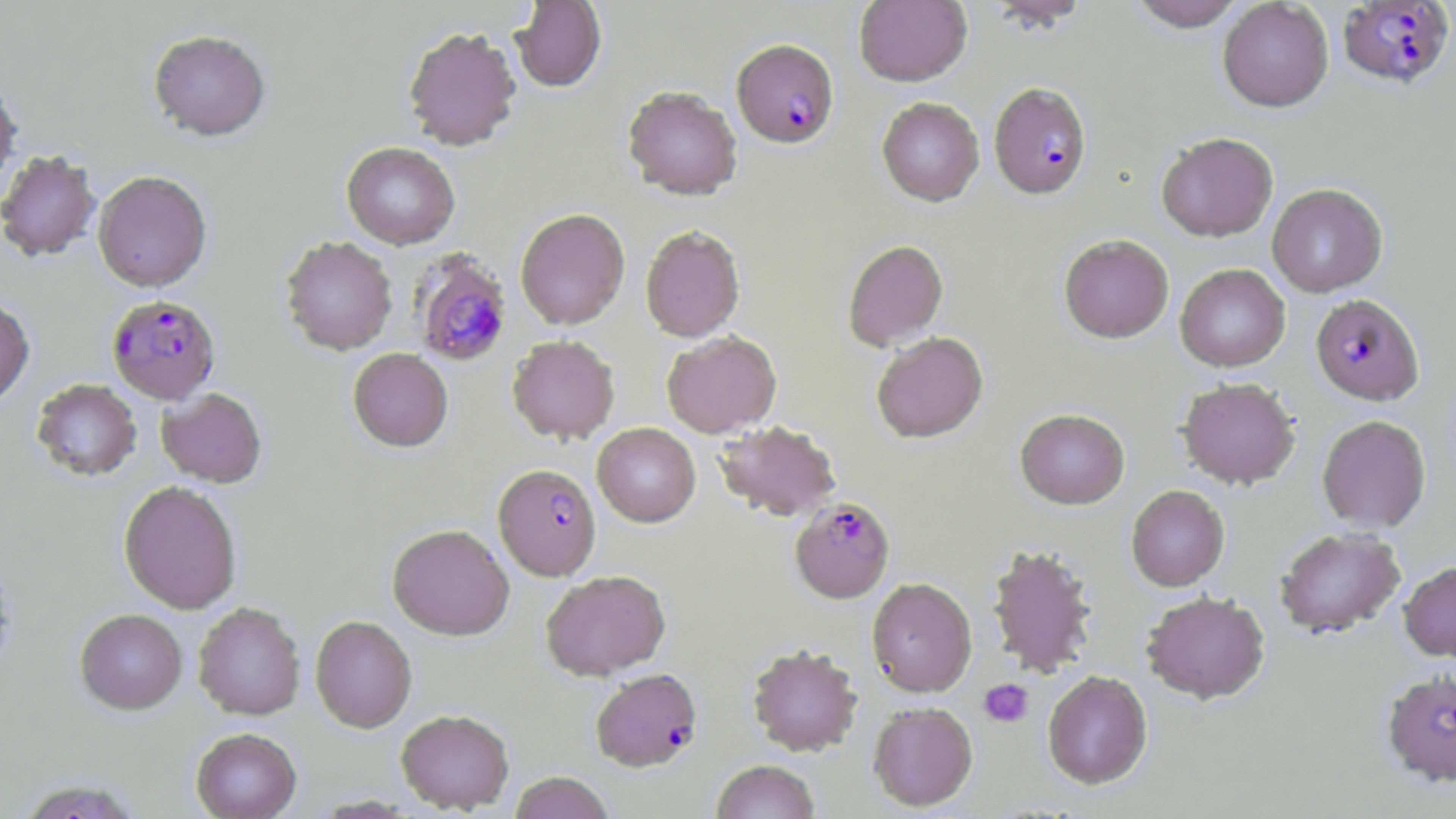
Approximate bounding boxes as (x1, y1, x2, y2) in pixels. Platelet locations: (979, 679, 1033, 727). Uninfected red blood cell locations: (510, 0, 606, 92), (854, 0, 972, 86), (983, 0, 1094, 29), (1127, 0, 1248, 31), (1218, 0, 1333, 112), (403, 26, 522, 151), (148, 29, 271, 141), (0, 79, 22, 195), (623, 85, 743, 199), (877, 97, 984, 206), (1156, 132, 1278, 241), (342, 143, 460, 249), (0, 150, 101, 262), (93, 170, 212, 292), (1267, 184, 1387, 297), (515, 208, 630, 330), (640, 225, 745, 342), (1059, 234, 1173, 342), (280, 236, 397, 354), (842, 239, 948, 350), (1175, 264, 1290, 372), (0, 296, 35, 409), (662, 331, 781, 437), (871, 332, 988, 443), (507, 334, 619, 444), (348, 348, 453, 452), (1177, 377, 1300, 489), (31, 378, 142, 482), (156, 389, 267, 488), (1014, 408, 1130, 509), (1317, 415, 1431, 532), (713, 420, 842, 521), (592, 422, 700, 527), (118, 481, 242, 614), (1126, 485, 1229, 591), (387, 524, 514, 640), (1274, 527, 1406, 638), (986, 543, 1099, 677), (1399, 560, 1456, 661), (541, 570, 670, 680), (866, 577, 977, 697), (1141, 591, 1270, 704), (193, 602, 305, 720), (75, 608, 188, 714), (310, 616, 417, 732), (747, 643, 862, 756), (1042, 670, 1152, 789), (868, 702, 977, 811), (396, 709, 514, 813), (191, 728, 301, 819), (711, 760, 820, 819), (509, 772, 615, 819), (15, 777, 146, 819). Plasmodium falciparum-infected red blood cell locations: (1338, 1, 1453, 89), (732, 39, 839, 148), (989, 82, 1092, 199), (409, 250, 513, 367), (1311, 294, 1424, 405), (107, 295, 220, 405), (493, 464, 601, 580), (790, 497, 894, 602), (591, 668, 702, 771), (1381, 670, 1456, 786). Slide-level diagnosis: Plasmodium falciparum. Thin blood film. Captured at 1000x magnification. Light microscopy. May-Grünwald-Giemsa-stained preparation. Single field of view. Image is 1456×819 pixels.